Classify this cell by malaria status.
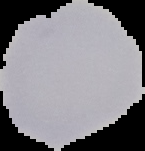
It is uninfected.

image type = segmented cell region with the area outside set to black
image size = 145×151 pixels
preparation = thin blood smear